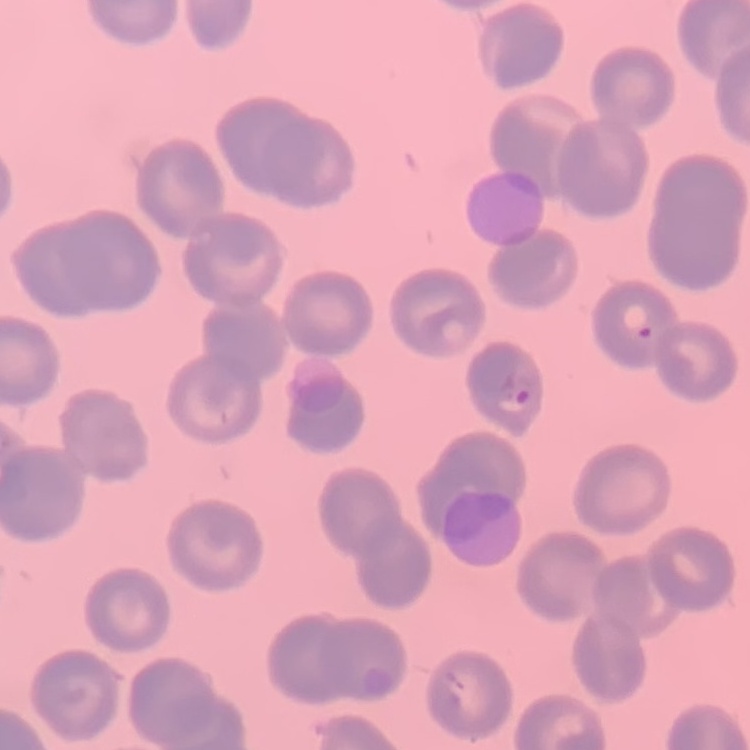

erythrocyte morphology = no rouleaux formation
image type = one tile cut from a larger photomicrograph
stain = Field's or Giemsa
preparation = thin peripheral smear